Outline each blood parasite and name the species.
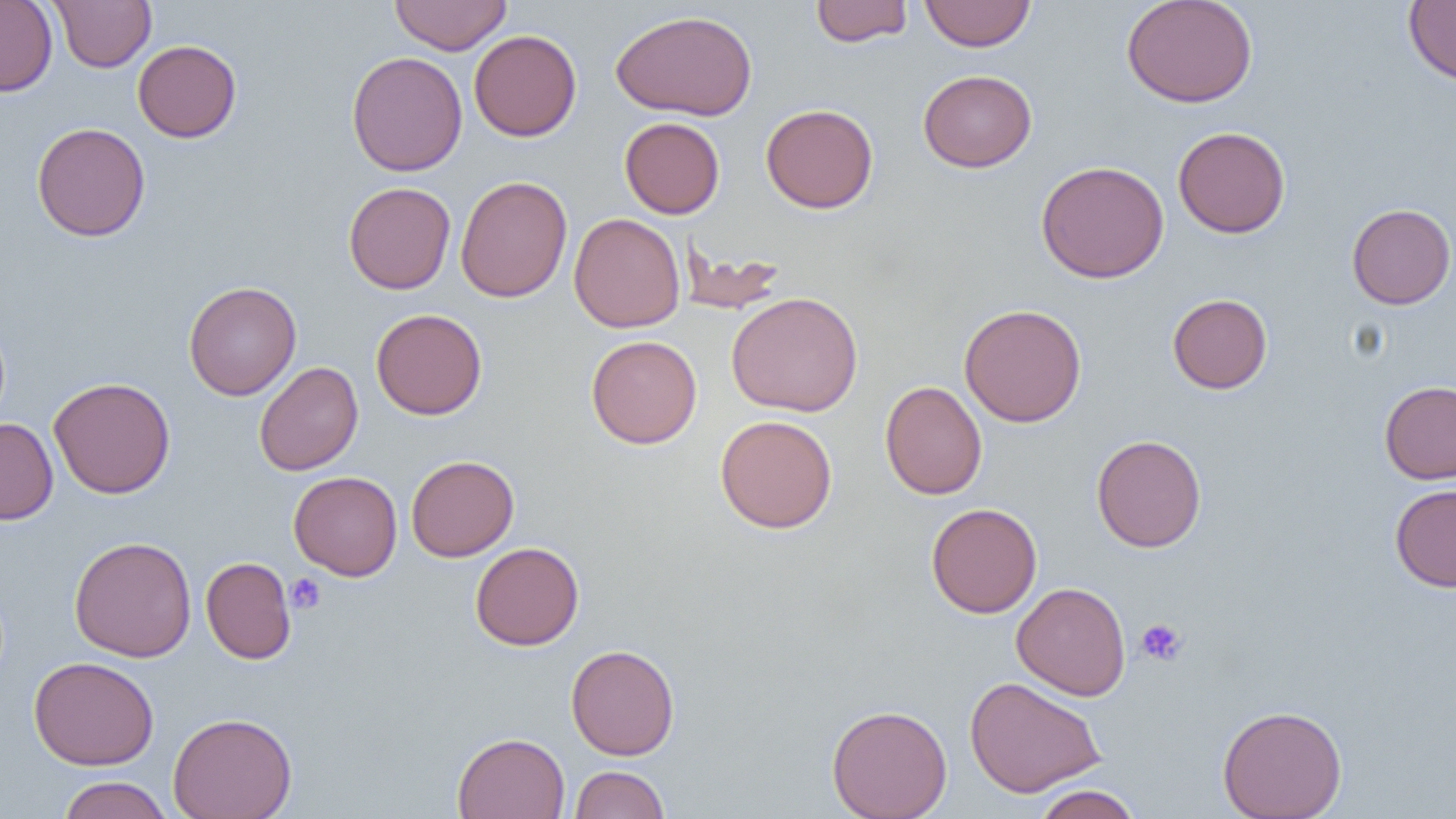

No blood parasites seen.

slide-level diagnosis = no evidence of blood parasites
uninfected red blood cell locations = approximate bounding boxes as [x1, y1, x2, y2] in pixels: [51, 0, 155, 72], [390, 0, 511, 55], [810, 0, 912, 47], [919, 0, 1035, 51], [1121, 0, 1258, 108], [0, 1, 58, 97], [1403, 1, 1456, 86], [611, 10, 758, 121], [469, 30, 582, 141], [132, 40, 242, 143], [347, 51, 468, 177], [918, 69, 1037, 172], [760, 103, 878, 213], [620, 117, 725, 219], [31, 122, 150, 241], [1173, 126, 1291, 238], [1035, 160, 1169, 283], [455, 175, 572, 302], [343, 181, 456, 294], [1346, 203, 1456, 309], [569, 213, 685, 333], [677, 243, 788, 316], [184, 281, 301, 400], [726, 291, 864, 417], [1167, 293, 1272, 394], [959, 303, 1087, 427], [371, 308, 488, 420], [586, 335, 702, 448], [254, 361, 363, 476], [48, 377, 176, 499], [1379, 380, 1456, 484], [880, 381, 987, 500], [715, 414, 838, 534], [0, 418, 58, 524], [1091, 434, 1206, 552], [406, 455, 519, 561], [288, 471, 402, 580], [1390, 483, 1456, 592], [926, 502, 1042, 618], [69, 536, 197, 662], [470, 541, 584, 651], [201, 557, 296, 664], [1011, 582, 1130, 700], [565, 644, 680, 760], [29, 655, 158, 771], [965, 676, 1106, 798], [827, 703, 952, 819], [1217, 704, 1347, 819], [168, 712, 297, 819], [453, 731, 570, 819], [569, 765, 669, 817], [57, 776, 173, 819], [1032, 784, 1143, 819]
modality = light microscopy
magnification = 1000x
image size = 1456×819 pixels
preparation = thin blood smear
field of view = one of a larger specimen
platelet locations = approximate bounding boxes as [x1, y1, x2, y2] in pixels: [286, 573, 327, 614], [1136, 618, 1187, 665]